State which parasite is depicted.
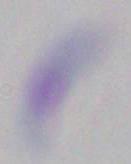
This is Toxoplasma gondii.

Summary:
  - Modality: photomicrograph
  - Magnification: 1000x